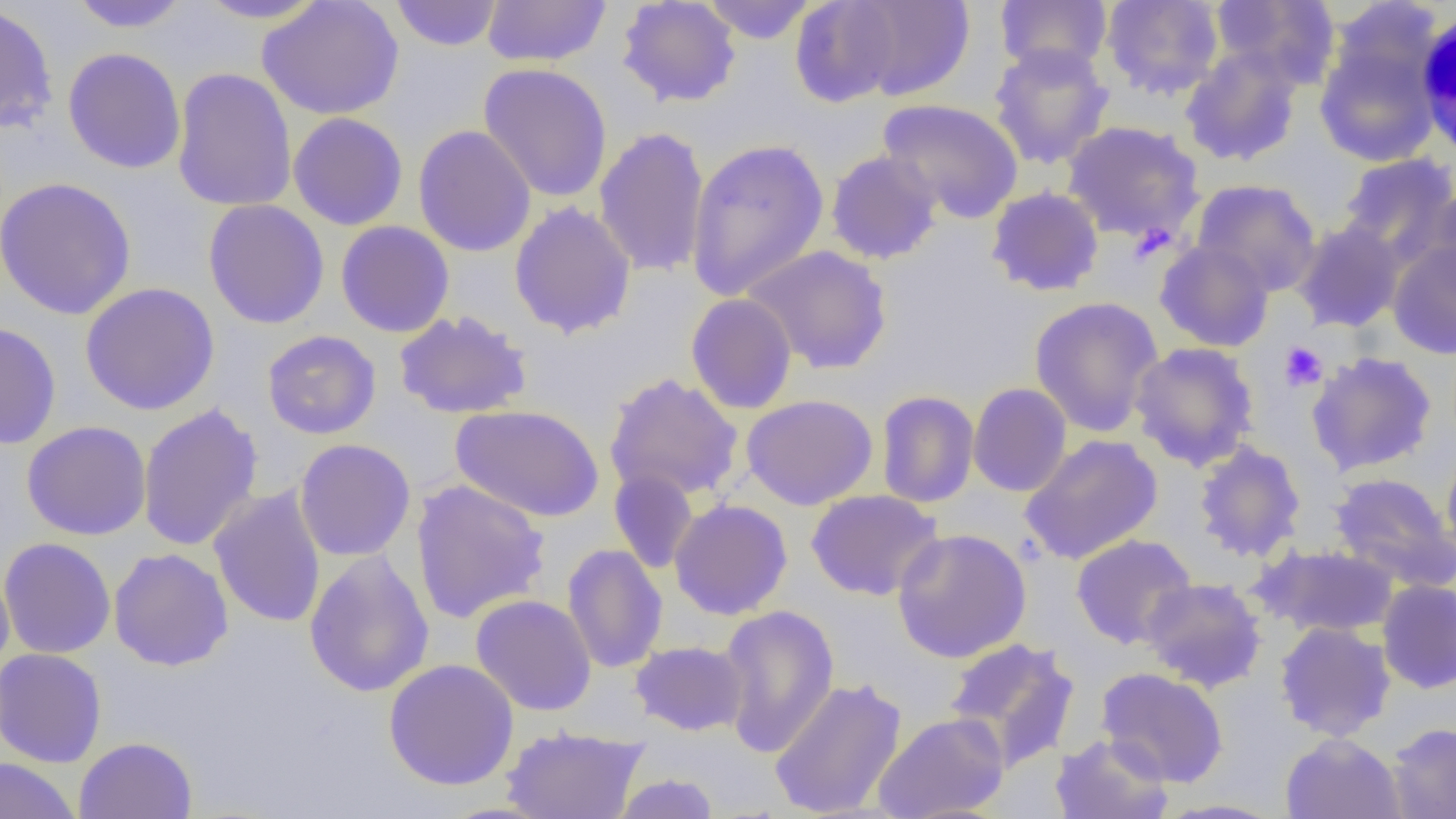
Approximate bounding boxes as (x1, y1, x2, y2) in pixels. Platelet locations: (1279, 341, 1328, 391). White blood cell locations: (1415, 6, 1456, 167). Uninfected red blood cell locations: (192, 0, 331, 24), (257, 0, 404, 120), (482, 0, 611, 68), (616, 0, 742, 108), (701, 0, 819, 44), (995, 0, 1112, 76), (1101, 0, 1224, 100), (1210, 0, 1341, 89), (67, 1, 192, 33), (390, 1, 504, 51), (789, 1, 904, 107), (843, 1, 976, 102), (0, 2, 58, 135), (1314, 37, 1440, 167), (988, 42, 1115, 170), (1180, 47, 1304, 167), (62, 48, 186, 174), (477, 63, 614, 203), (171, 67, 297, 213), (878, 98, 1024, 223), (288, 112, 408, 231), (1061, 120, 1205, 245), (413, 124, 537, 257), (593, 126, 711, 277), (685, 137, 830, 302), (825, 150, 943, 264), (1337, 152, 1456, 264), (0, 176, 138, 320), (1191, 179, 1322, 296), (986, 186, 1105, 297), (1420, 187, 1456, 306), (203, 199, 330, 329), (509, 201, 637, 339), (1291, 220, 1405, 333), (336, 221, 455, 337), (1386, 237, 1456, 359), (1154, 239, 1275, 352), (743, 245, 893, 375), (79, 282, 220, 415), (686, 293, 797, 414), (1028, 295, 1164, 437), (393, 310, 532, 420), (0, 321, 62, 449), (262, 330, 381, 439), (1129, 341, 1260, 471), (1306, 351, 1438, 477), (603, 373, 744, 502), (968, 382, 1072, 497), (876, 390, 980, 508), (741, 394, 878, 510), (137, 403, 264, 552), (450, 403, 605, 523), (21, 421, 152, 541), (1020, 433, 1163, 565), (295, 438, 415, 561), (1192, 439, 1307, 564), (1441, 443, 1456, 562), (609, 469, 699, 574), (1329, 472, 1455, 593), (410, 480, 550, 624), (209, 485, 326, 629), (805, 489, 944, 601), (669, 499, 793, 620), (892, 528, 1031, 663), (1070, 533, 1197, 650), (0, 537, 116, 659), (562, 543, 668, 674), (1253, 543, 1400, 639), (108, 547, 234, 671), (303, 549, 435, 698), (0, 564, 15, 675), (1140, 577, 1267, 693), (1377, 579, 1456, 694), (471, 594, 597, 716), (717, 603, 839, 758), (1274, 621, 1397, 741), (944, 637, 1080, 772), (630, 640, 748, 736), (0, 647, 107, 768), (383, 658, 520, 790), (1095, 667, 1229, 787), (768, 676, 907, 818), (873, 711, 1010, 819), (1386, 722, 1456, 818), (501, 725, 649, 819), (1279, 732, 1407, 819), (1050, 733, 1175, 819), (74, 736, 197, 819), (0, 757, 82, 819), (611, 772, 721, 819), (1155, 798, 1289, 818). Slide-level diagnosis: negative for blood parasites. Light microscopy. Single field of view. Image is 1456×819 pixels. Thin blood smear. Captured at 1000x magnification.